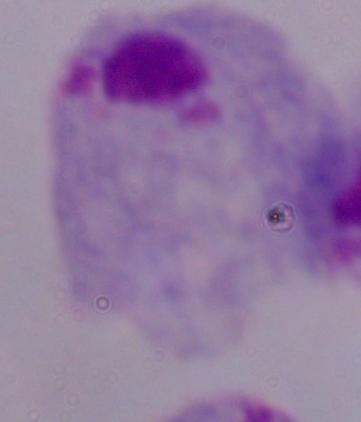
A trichomonad is seen. Micrograph. 1000x magnification.